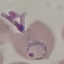
Summary:
  - Malaria status: parasitized
  - Capture: smartphone through the microscope eyepiece
  - Preparation: thin blood film
  - Stain: Giemsa
  - Image type: cell patch, automatically extracted from a larger field of view and resized to 64 × 64 pixels